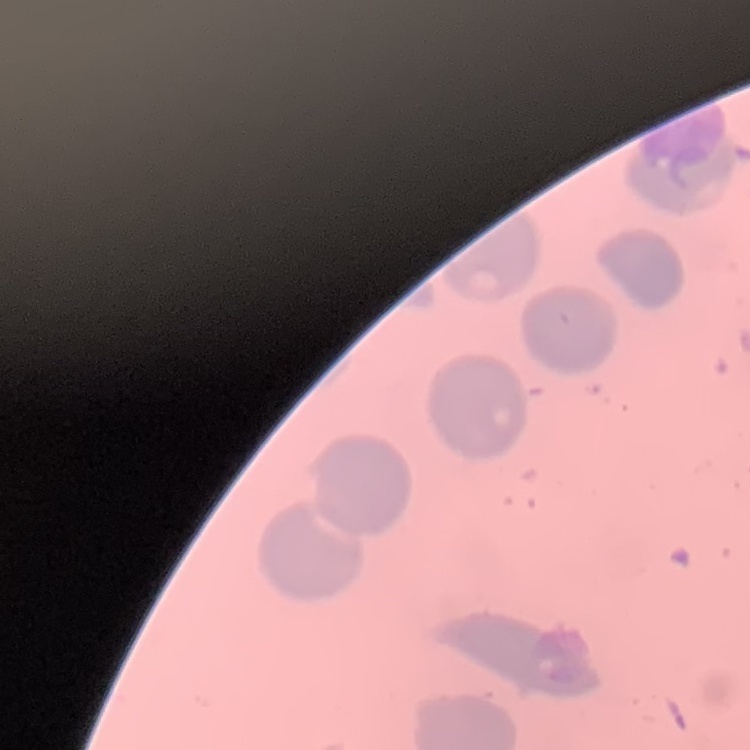
Summary:
  - Red blood cell morphology: no rouleaux formation
  - Preparation: thin blood smear
  - Image type: one tile cut from a larger photomicrograph
  - Stain: Field's or Giemsa